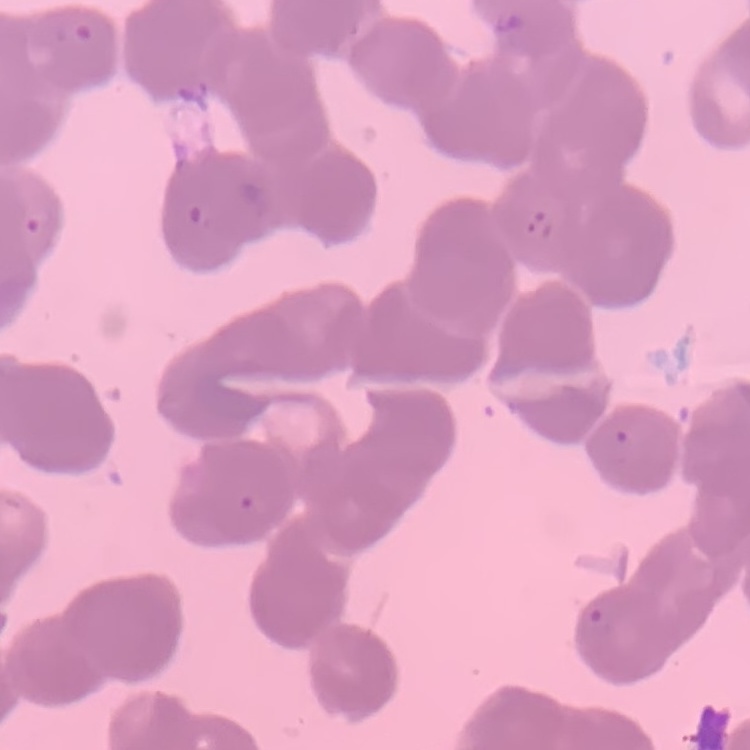

Summary:
  - Red blood cell morphology: rouleaux formation
  - Image type: square crop of a larger photomicrograph
  - Stain: Field's or Giemsa
  - Preparation: thin blood film